Locate every blood parasite and identify its species.
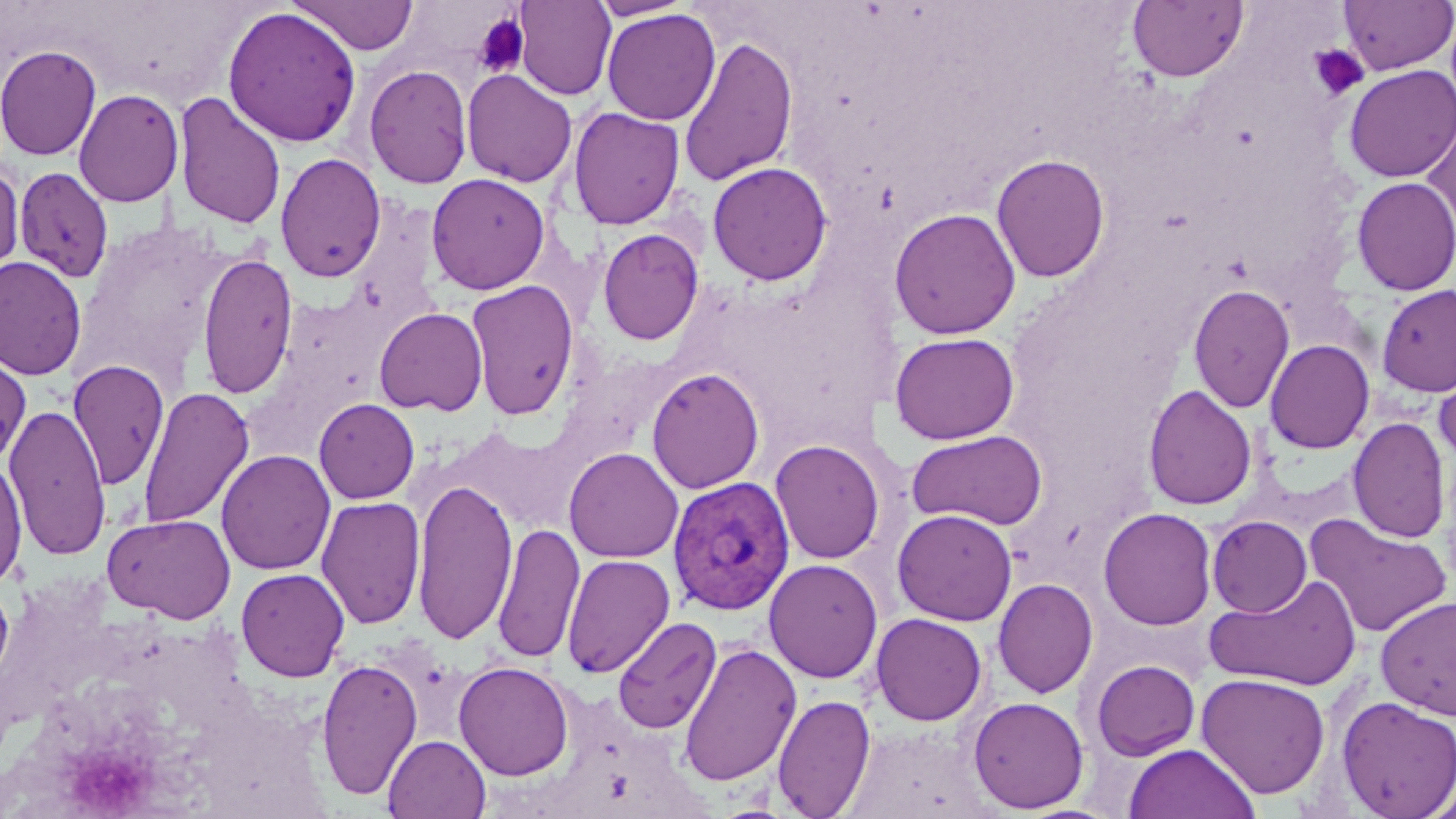
Approximate bounding boxes as [x1, y1, x2, y2] in pixels.
Plasmodium vivax-infected red blood cells: [668, 476, 797, 617].
No Plasmodium falciparum, Plasmodium ovale, Plasmodium malariae, Babesia divergens, or Trypanosoma brucei observed.

Summary:
  - Platelet locations: [473, 13, 529, 77], [1307, 44, 1369, 102]
  - Uninfected red blood cell locations: [290, 0, 418, 55], [514, 0, 616, 100], [1337, 0, 1455, 75], [588, 1, 698, 21], [1128, 1, 1248, 83], [222, 6, 362, 148], [602, 8, 721, 125], [679, 35, 798, 188], [0, 44, 102, 160], [364, 64, 473, 189], [1343, 64, 1456, 182], [461, 68, 577, 188], [73, 88, 184, 207], [172, 91, 287, 230], [568, 106, 685, 230], [1422, 108, 1456, 247], [275, 153, 386, 283], [991, 153, 1111, 283], [707, 161, 832, 285], [0, 163, 24, 279], [15, 166, 115, 283], [426, 172, 550, 294], [1351, 176, 1456, 296], [888, 207, 1021, 339], [597, 228, 705, 345], [197, 251, 298, 398], [0, 255, 87, 381], [466, 280, 579, 420], [1188, 283, 1295, 413], [1376, 284, 1456, 397], [373, 307, 488, 416], [889, 332, 1018, 445], [1264, 339, 1375, 454], [0, 349, 32, 468], [68, 360, 170, 490], [646, 367, 765, 494], [1434, 367, 1456, 468], [1143, 384, 1258, 510], [138, 386, 254, 530], [314, 398, 420, 504], [4, 403, 111, 561], [1347, 417, 1450, 543], [448, 426, 577, 534], [907, 429, 1048, 530], [769, 439, 886, 564], [563, 447, 684, 563], [216, 449, 336, 575], [0, 458, 27, 589], [412, 476, 517, 645], [315, 495, 426, 629], [1098, 507, 1217, 630], [892, 508, 1017, 626], [102, 513, 236, 623], [1304, 514, 1453, 638], [1207, 515, 1312, 617], [492, 522, 585, 664], [561, 553, 675, 678], [763, 558, 884, 683], [235, 567, 349, 682], [1204, 574, 1363, 692], [0, 577, 14, 689], [992, 577, 1098, 698], [1375, 594, 1456, 719], [870, 613, 987, 726], [613, 617, 722, 734], [679, 642, 801, 787], [316, 657, 423, 801], [1090, 659, 1201, 762], [453, 661, 575, 781], [1196, 673, 1330, 799], [771, 694, 876, 818], [967, 696, 1089, 814], [1336, 696, 1456, 818], [384, 735, 490, 819], [1124, 743, 1260, 819], [1421, 783, 1456, 819]
  - Slide-level diagnosis: Plasmodium vivax
  - Preparation: thin blood film
  - Modality: optical microscopy
  - Magnification: 1000x
  - Stain: May-Grünwald-Giemsa
  - Field of view: single
  - Image size: 1456×819 pixels